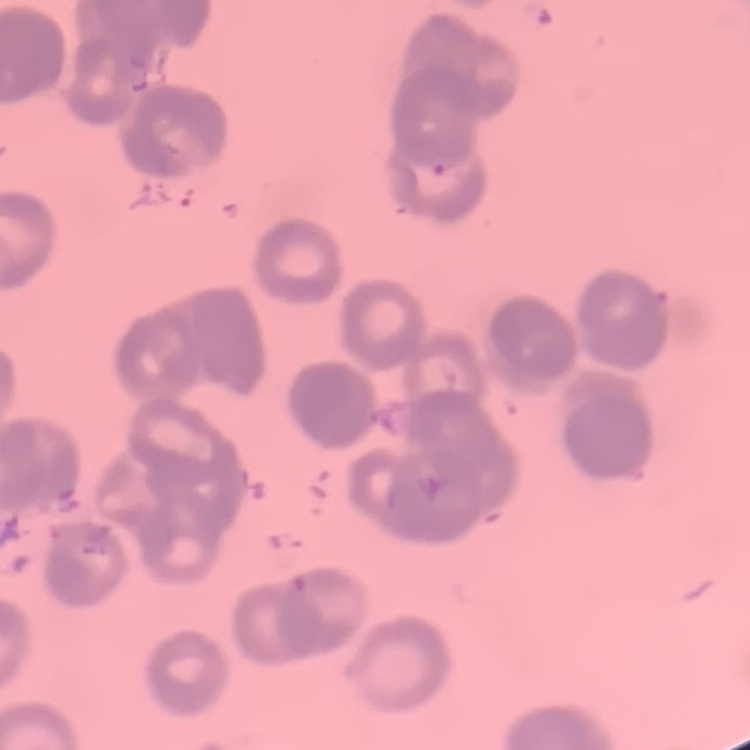
The erythrocytes show rouleaux formation. Square crop of a larger photomicrograph. Thin peripheral smear. Field's or Giemsa stain.